Give the position of every Plasmodium parasite visible.
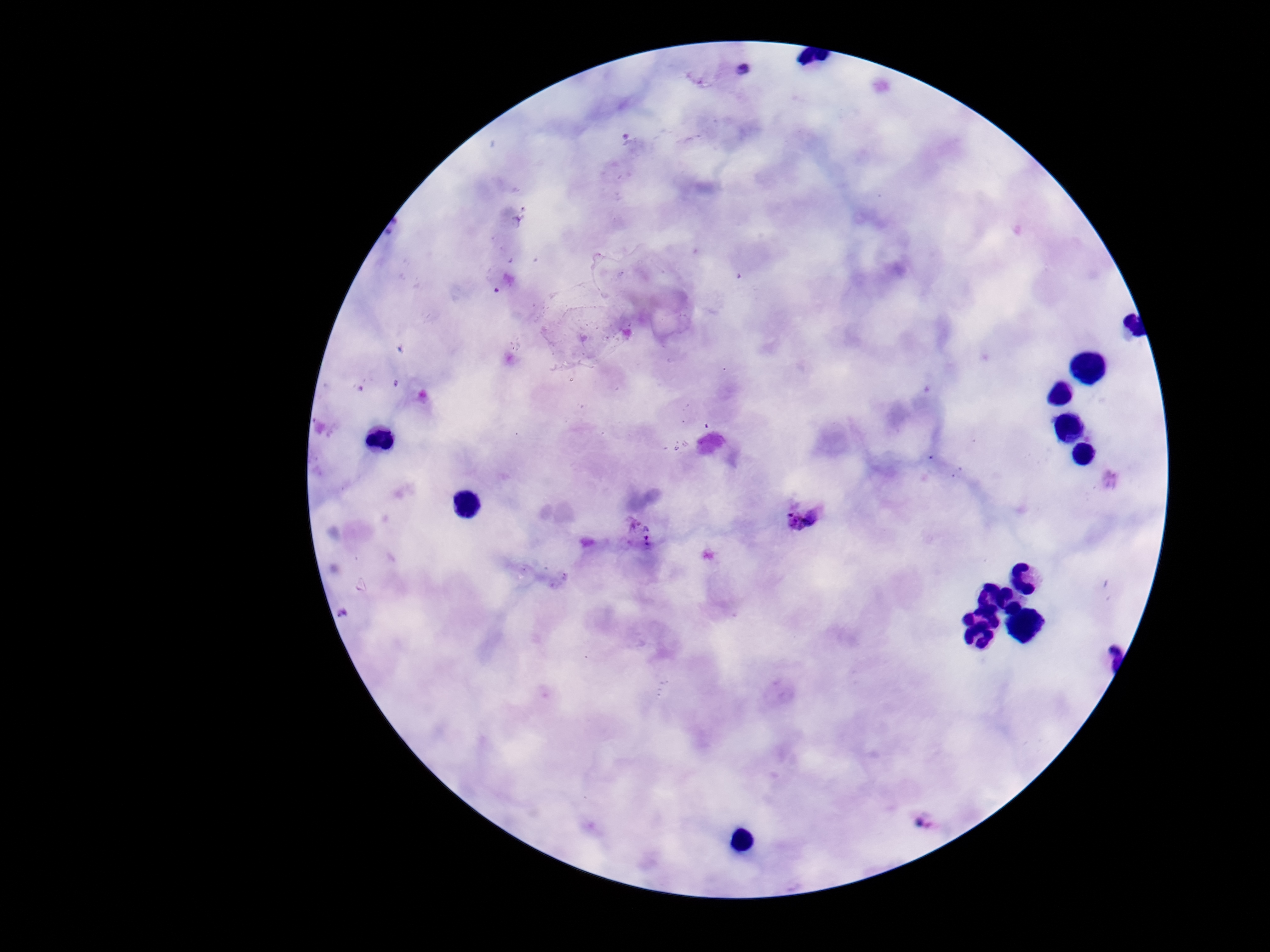

Approximate object centers, in pixels from the top-left corner.
Plasmodium parasites: (x=803, y=516), (x=636, y=531).

{
  "patient_malaria_status": "infected",
  "capture": "smartphone camera through the microscope eyepiece",
  "preparation": "thick blood smear",
  "image_size": "1270×952 pixels",
  "magnification": "100x",
  "stain": "Giemsa",
  "field_of_view": "one from this slide"
}